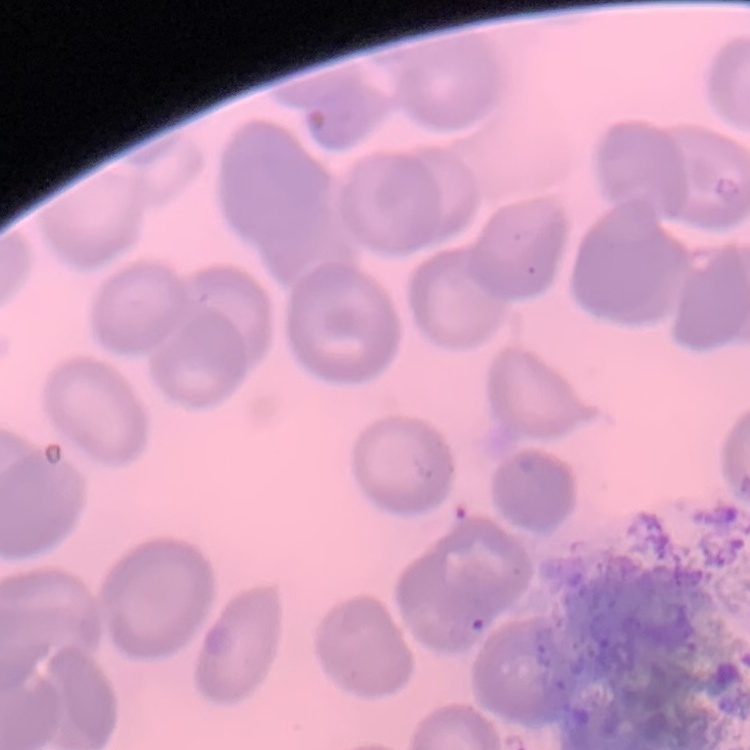

Summary:
  - Erythrocyte morphology: no rouleaux formation
  - Preparation: thin peripheral smear
  - Stain: Field's or Giemsa
  - Image type: square crop of a larger photomicrograph